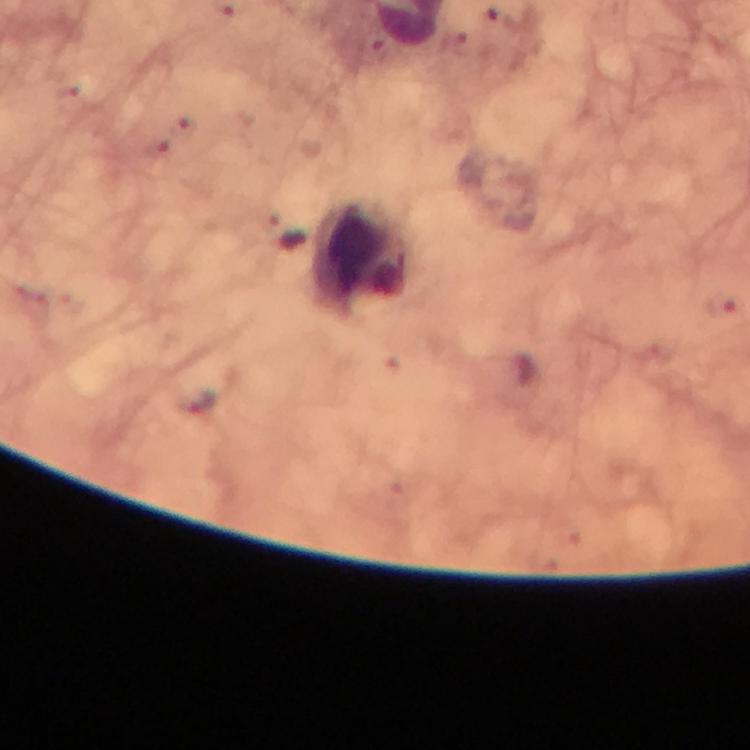

Approximate object centers, in pixels from the top-left corner. Leukocyte locations: (x=363, y=254). Malaria parasite locations: (x=498, y=18). Giemsa-stained preparation. From a diagnostic examination for malaria. Photographed with a smartphone mounted on the microscope. Thick smear. Image is 750×750 pixels. Immersion oil was used. Cropped region of a single field of view. At 100x magnification.